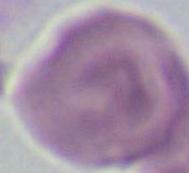

Captured at 1000x magnification. Photomicrograph. A red blood cell is shown.